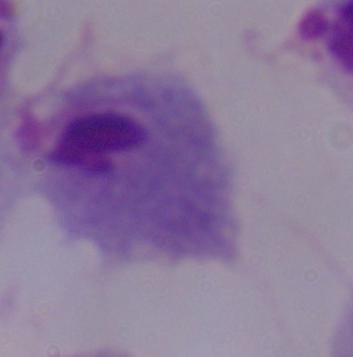

Summary:
  - Magnification: 1000x
  - Modality: photomicrograph
  - Identification: trichomonad